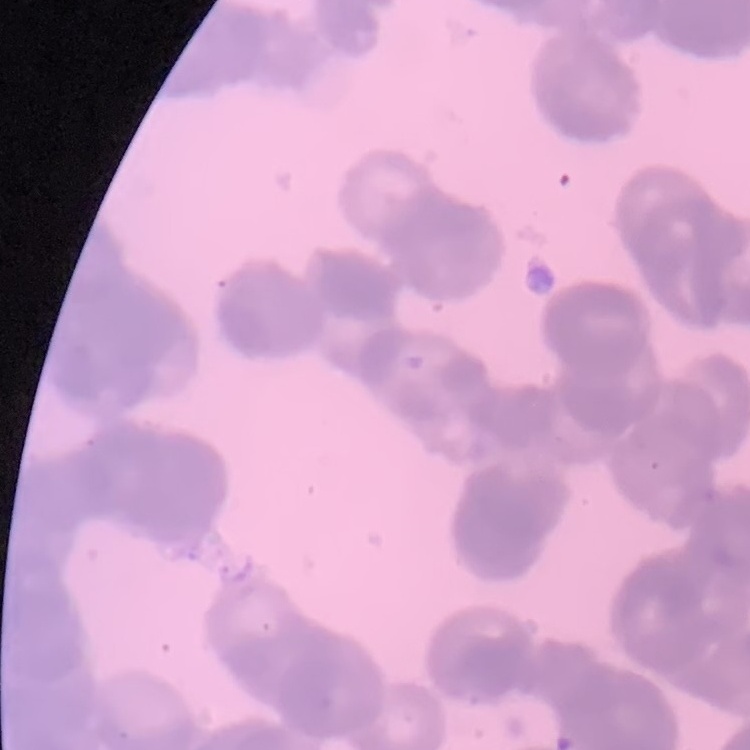
The red blood cells exhibit rouleaux formation. One tile cut from a larger photomicrograph. Field's or Giemsa stain. Thin blood smear.